Give the extent of all uninfected red blood cells.
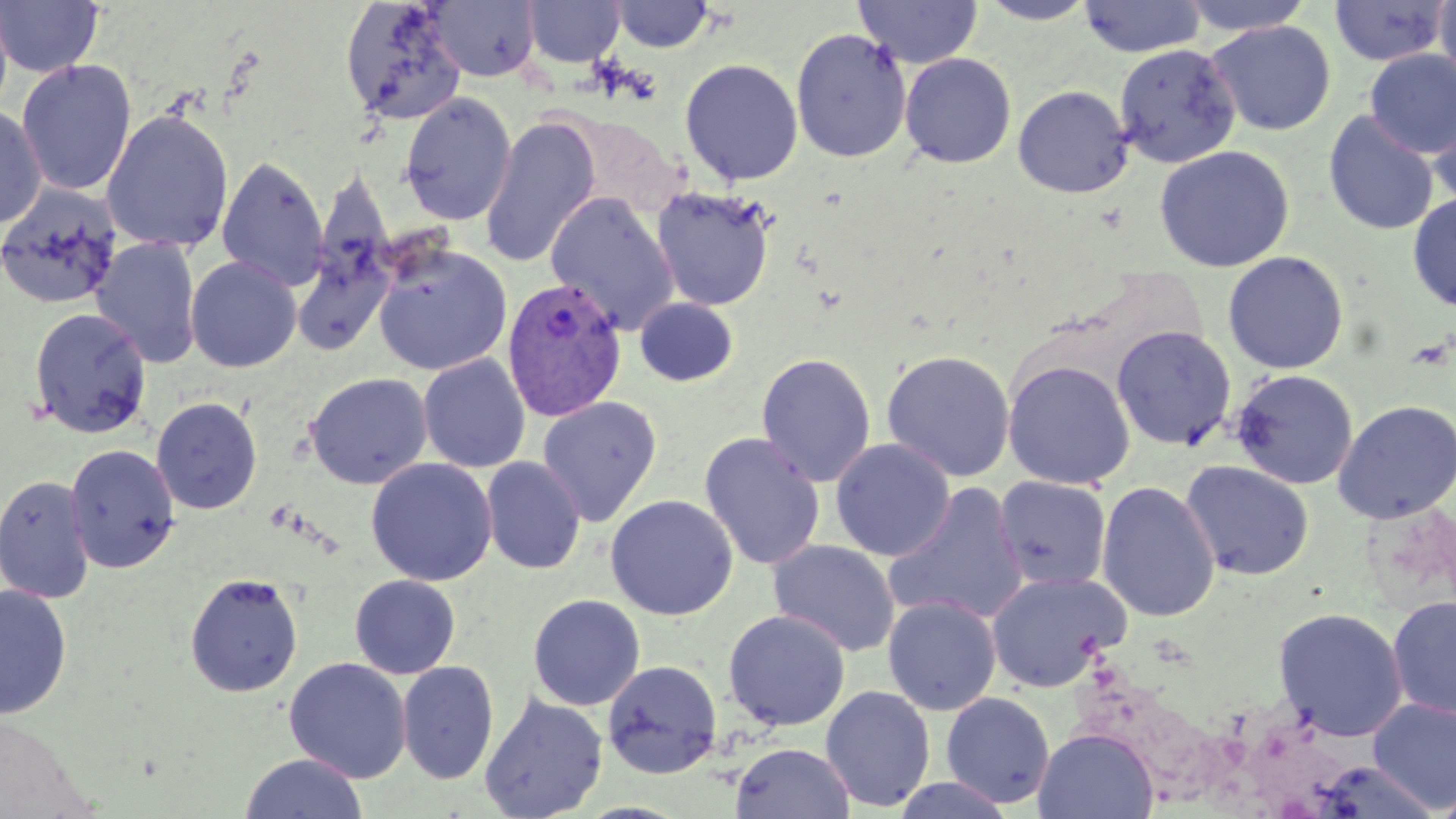

Approximate bounding boxes as (x1, y1, x2, y2) in pixels.
Uninfected red blood cells: (0, 0, 14, 123), (0, 0, 104, 78), (428, 0, 540, 82), (854, 0, 982, 68), (976, 0, 1100, 25), (1078, 0, 1206, 58), (1178, 0, 1316, 36), (1433, 0, 1456, 89), (340, 1, 467, 125), (523, 1, 624, 67), (610, 1, 716, 52), (1328, 1, 1451, 67), (1205, 20, 1337, 136), (790, 28, 912, 163), (1114, 43, 1240, 168), (1364, 49, 1456, 158), (900, 53, 1016, 168), (16, 58, 138, 197), (680, 58, 803, 185), (1013, 85, 1133, 198), (399, 93, 517, 226), (1428, 99, 1456, 211), (0, 102, 47, 228), (101, 108, 234, 253), (1323, 110, 1440, 236), (558, 113, 684, 219), (480, 115, 601, 269), (1154, 144, 1294, 273), (216, 155, 329, 291), (0, 182, 123, 311), (651, 188, 775, 310), (1408, 192, 1456, 313), (545, 193, 680, 335), (292, 235, 395, 357), (92, 236, 203, 369), (373, 243, 512, 376), (1222, 251, 1349, 374), (185, 256, 302, 373), (635, 297, 738, 387), (28, 307, 151, 438), (1111, 326, 1237, 451), (881, 349, 1016, 482), (756, 353, 876, 487), (418, 354, 531, 473), (1001, 359, 1136, 490), (1229, 368, 1358, 490), (305, 372, 433, 489), (151, 396, 263, 515), (537, 396, 662, 526), (1332, 399, 1456, 524), (700, 433, 825, 571), (830, 438, 955, 561), (65, 443, 179, 573), (481, 456, 586, 574), (365, 458, 498, 586), (1180, 460, 1315, 581), (0, 474, 96, 603), (994, 476, 1112, 592), (1096, 480, 1220, 623), (884, 484, 1029, 627), (605, 494, 738, 620), (767, 539, 901, 657), (986, 571, 1131, 693), (184, 572, 303, 697), (350, 574, 460, 679), (0, 584, 73, 720), (528, 594, 645, 711), (883, 595, 1001, 716), (1387, 596, 1456, 722), (1273, 606, 1408, 741), (722, 610, 850, 731), (284, 657, 412, 783), (602, 660, 722, 778), (397, 661, 498, 784), (821, 685, 936, 812), (941, 691, 1055, 808), (480, 693, 608, 818), (1368, 698, 1456, 812), (1034, 728, 1158, 819), (731, 742, 855, 819), (239, 753, 368, 819), (890, 776, 1016, 818), (1437, 776, 1456, 819).

slide_level_diagnosis: Plasmodium vivax
preparation: thin blood film
magnification: 1000x
modality: light microscopy
image_size: 1456×819 pixels
plasmodium_vivax_infected_red_blood_cell_locations: 'approximate bounding boxes as (x1, y1, x2, y2) in pixels: (502, 277, 627, 422)'
field_of_view: single
stain: May-Grünwald-Giemsa